Report the malaria status of this cell.
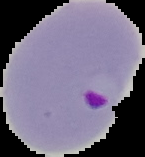

Parasitized.

image type = segmented cell region on a black background
preparation = thin blood film
image size = 145×157 pixels